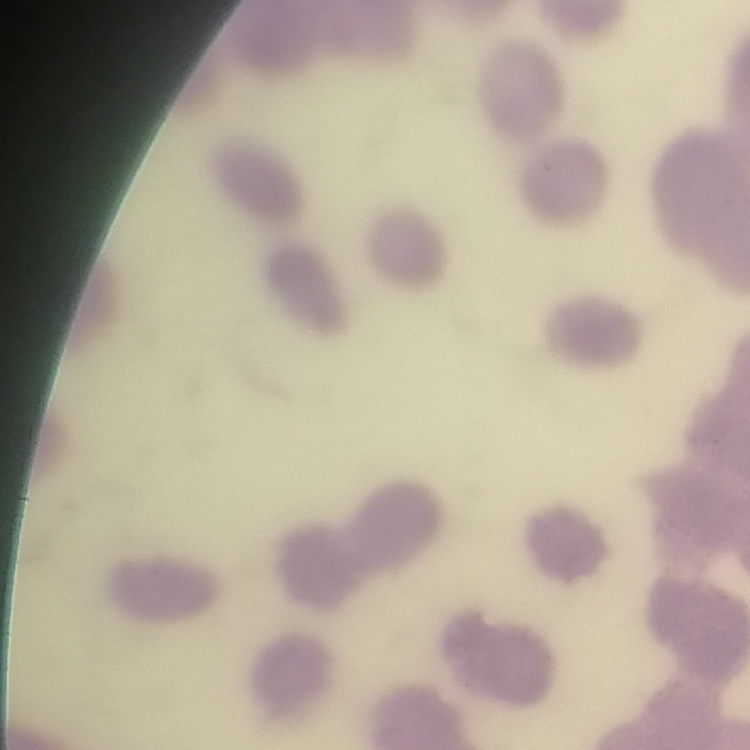 The erythrocytes exhibit rouleaux formation. Thin blood smear. One tile cut from a larger photomicrograph. Field's or Giemsa stain.